Name the parasite shown.
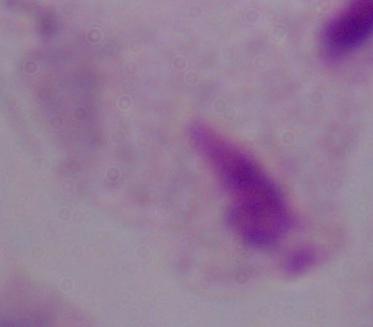
A trichomonad.

Photomicrograph. Captured at 1000x magnification.